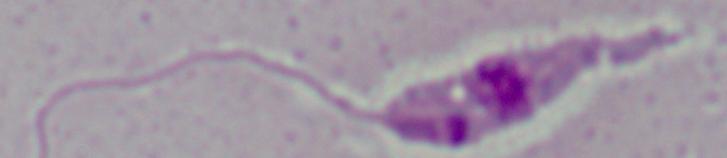

Summary:
  - Identification: Leishmania
  - Magnification: 1000x
  - Modality: photomicrograph